Assess this cell for malaria.
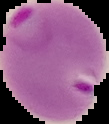
Parasitized.

image size = 109×124 pixels
image type = segmented cell region with the area outside set to black
preparation = thin blood film